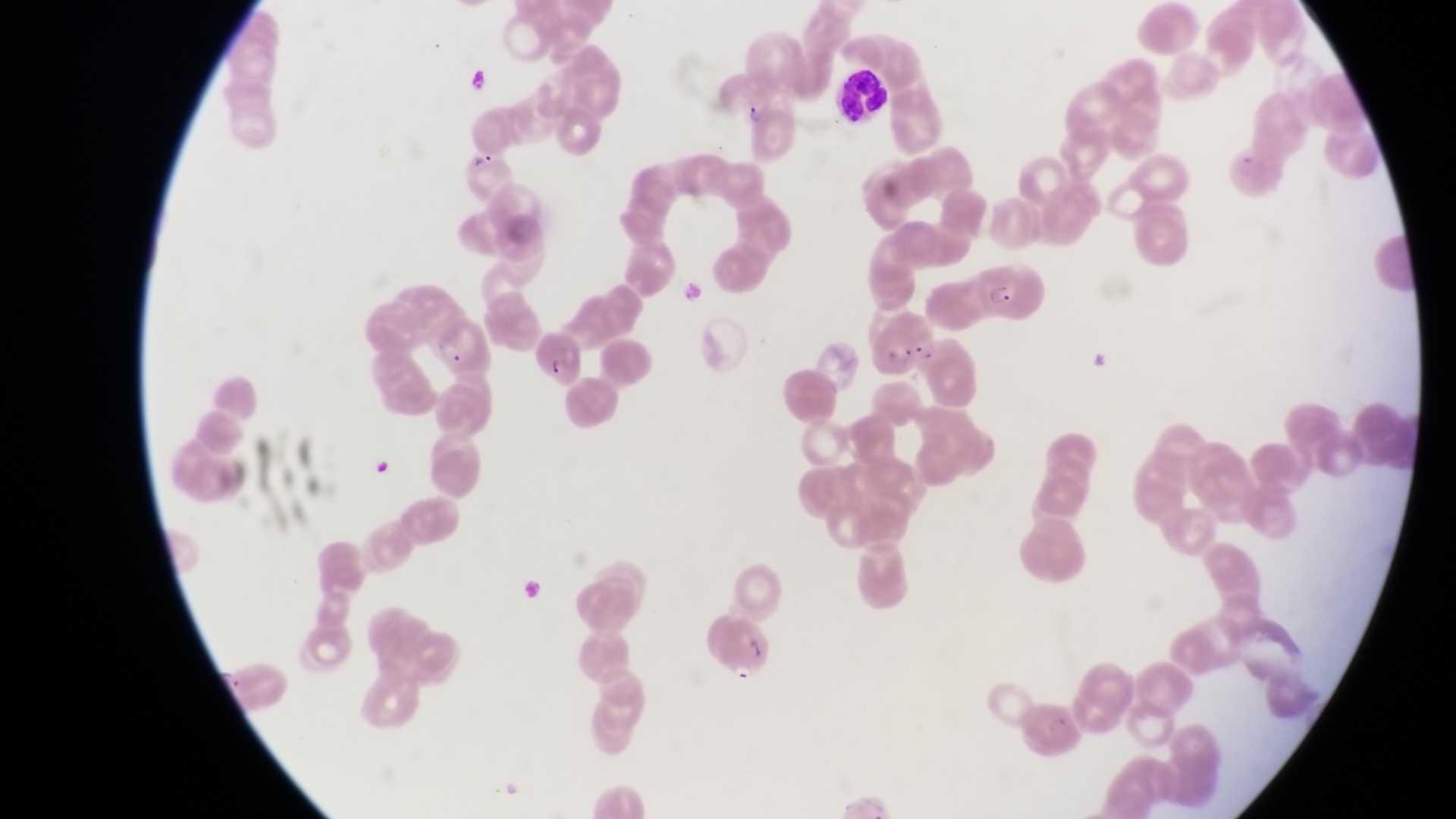

Approximate bounding boxes as [left, top, right, bottom] in pixels.
Summary:
  - Leukocyte locations: [835, 67, 893, 125]
  - Trophozoite locations: [460, 64, 489, 97], [737, 95, 763, 125]
  - Artifact (platelet-like body, stain precipitate, or debris) locations: [1224, 145, 1287, 204], [463, 146, 487, 167]
  - Parasitised red blood cell locations: [973, 264, 1050, 328], [532, 327, 582, 387], [704, 618, 771, 679]
  - Capture: smartphone photograph through the eyepiece of an Olympus CX-23 microscope
  - Country: Uganda
  - Image size: 1456×819 pixels
  - Preparation: thin blood film
  - Magnification: 1000x
  - Field of view: single